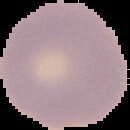

Summary:
  - Preparation: thin blood film
  - Malaria status: uninfected
  - Image type: cell region segmented out of the field of view; surrounding area masked to black
  - Image size: 130×130 pixels